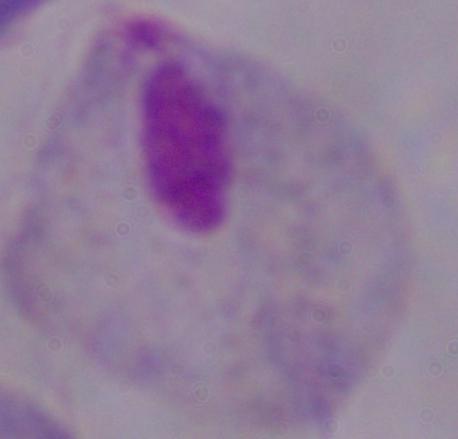
Micrograph. 1000x magnification. A trichomonad is seen.